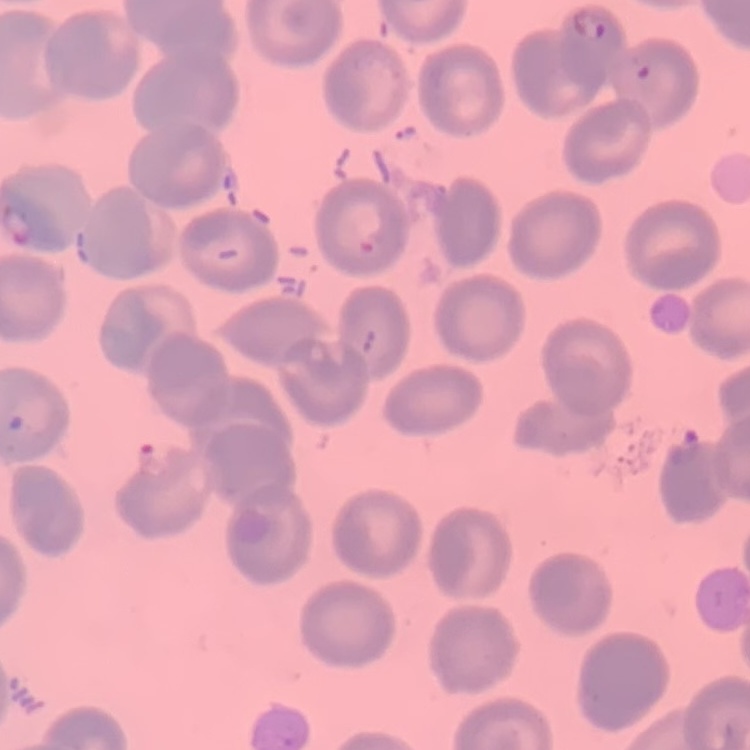
Summary:
  - Red blood cell morphology: no rouleaux formation
  - Image type: square crop of a larger photomicrograph
  - Stain: Field's or Giemsa
  - Preparation: thin peripheral smear